Comment on the morphology of the red blood cells.
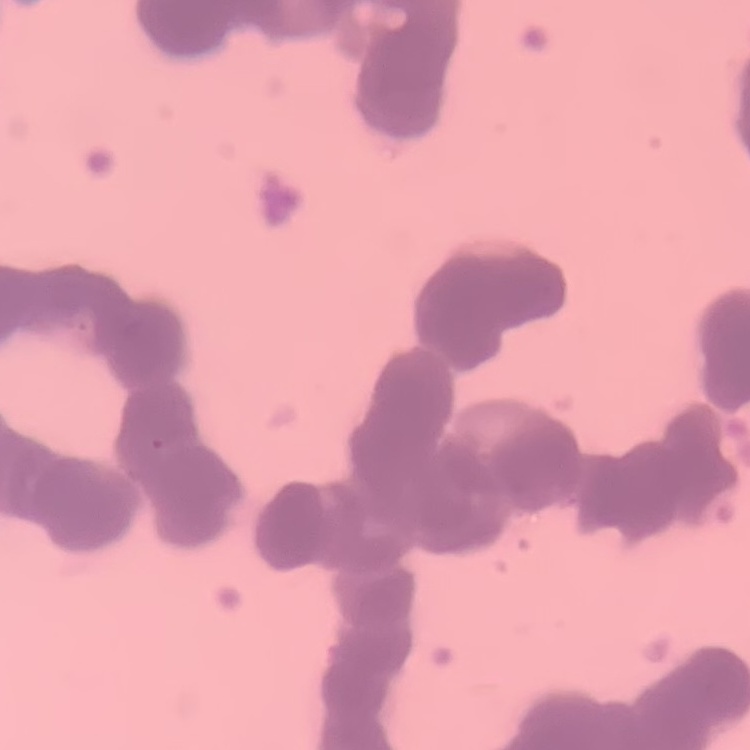

Rouleaux formation.

image type = square crop of a larger photomicrograph
stain = Field's or Giemsa
preparation = thin blood smear